Assess the morphology of the red blood cells.
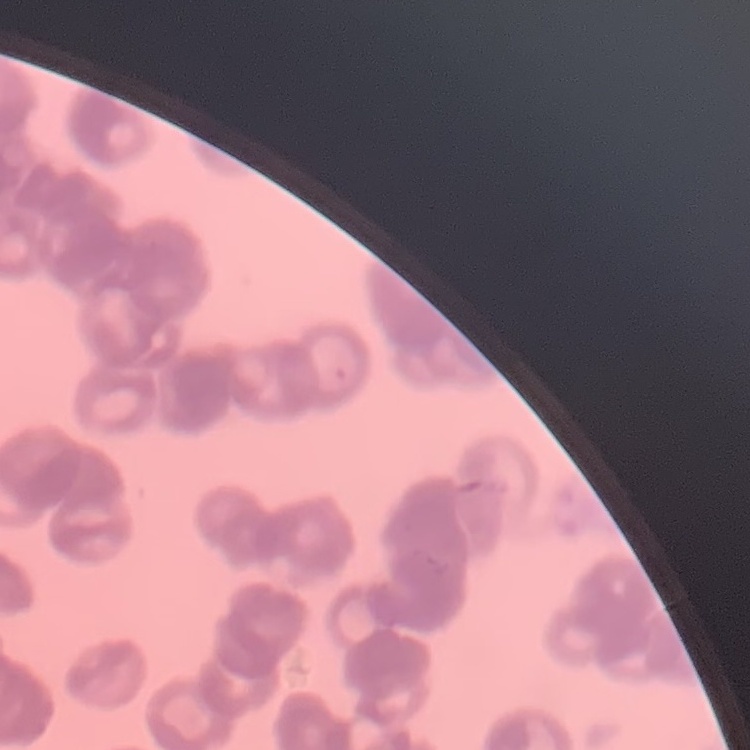

They show rouleaux formation.

stain = Field's or Giemsa
preparation = thin blood smear
image type = one tile cut from a larger photomicrograph